Identify the parasite.
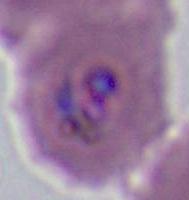

Plasmodium.

400x or 1000x magnification. Micrograph.